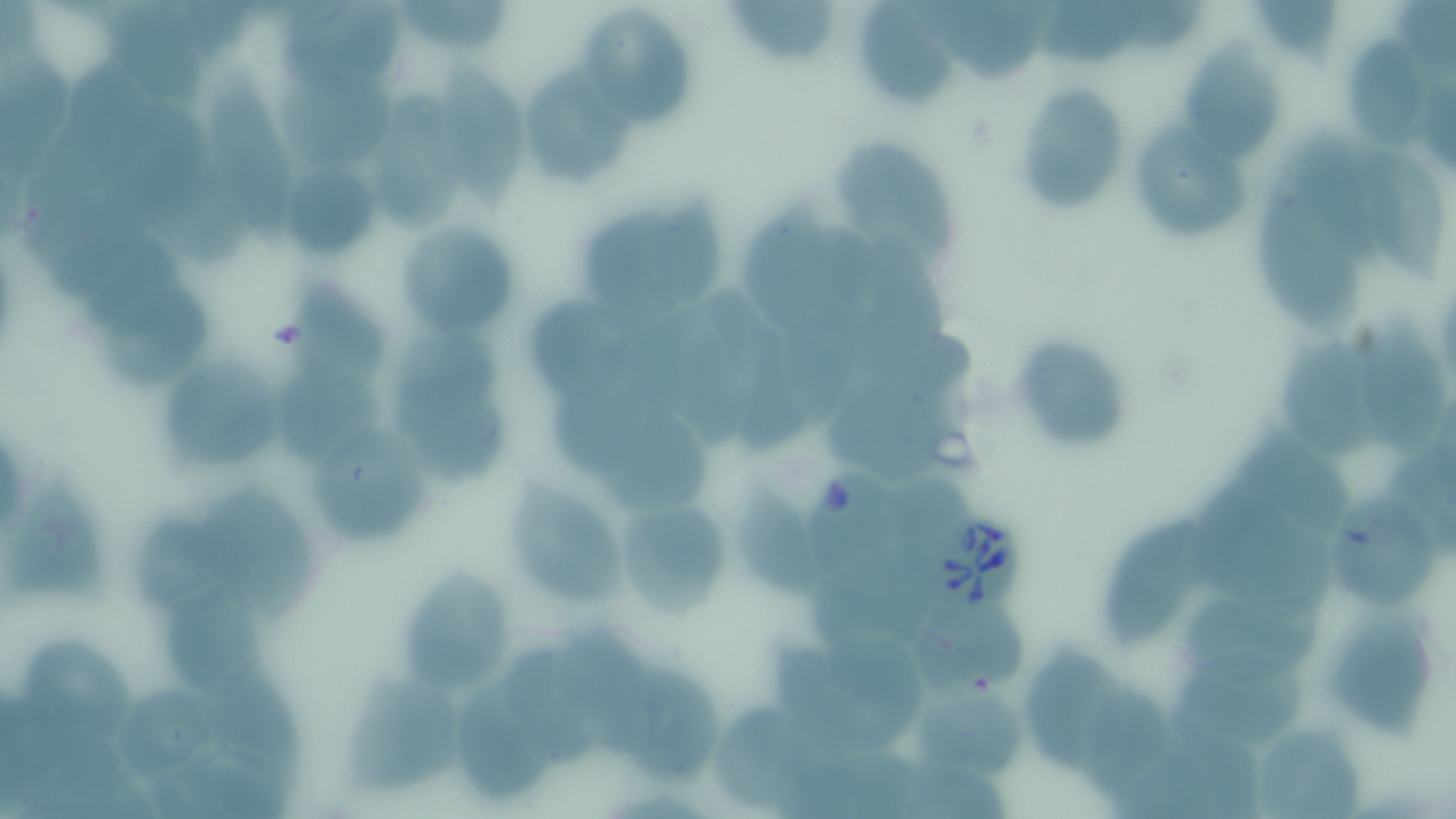 Approximate bounding boxes as [x1, y1, x2, y2] in pixels. Uninfected red blood cell locations: [105, 0, 204, 105], [723, 0, 844, 64], [931, 0, 1043, 84], [1037, 0, 1149, 69], [1258, 0, 1345, 69], [853, 1, 966, 104], [280, 3, 403, 87], [401, 3, 515, 53], [1114, 3, 1207, 51], [582, 6, 691, 126], [1346, 33, 1434, 149], [1173, 38, 1290, 161], [67, 54, 166, 173], [439, 58, 523, 214], [276, 61, 392, 168], [526, 64, 637, 183], [210, 67, 297, 259], [1010, 77, 1124, 212], [373, 93, 471, 229], [109, 98, 207, 219], [1135, 123, 1248, 240], [1294, 135, 1385, 273], [829, 138, 959, 262], [1342, 140, 1447, 283], [1255, 182, 1365, 331], [747, 195, 836, 333], [580, 197, 720, 305], [392, 218, 510, 334], [85, 226, 183, 327], [865, 237, 956, 379], [282, 279, 397, 388], [101, 280, 213, 387], [535, 293, 647, 400], [783, 298, 864, 424], [1364, 315, 1443, 460], [741, 325, 810, 455], [1284, 330, 1388, 465], [1012, 335, 1128, 450], [156, 351, 285, 472], [272, 365, 381, 464], [393, 371, 512, 484], [545, 379, 657, 476], [824, 393, 964, 482], [617, 398, 709, 522], [1235, 421, 1356, 538], [312, 423, 431, 546], [1192, 473, 1315, 587], [893, 475, 970, 567], [4, 479, 111, 604], [504, 480, 628, 607], [731, 481, 823, 602], [202, 486, 322, 625], [1321, 490, 1437, 607], [620, 502, 726, 625], [125, 510, 238, 620], [1101, 510, 1216, 649], [399, 565, 511, 692], [155, 593, 275, 698], [910, 593, 1035, 697], [1183, 593, 1323, 677], [1330, 606, 1435, 740], [816, 622, 927, 750], [558, 629, 643, 756], [1181, 637, 1310, 747], [19, 638, 142, 750], [497, 638, 593, 769], [1022, 638, 1132, 776], [771, 642, 872, 756], [605, 656, 719, 785], [197, 661, 315, 790], [338, 675, 467, 794], [117, 681, 210, 782], [457, 682, 551, 805], [1076, 682, 1174, 795], [917, 686, 1024, 781], [712, 703, 817, 809], [1248, 719, 1367, 817], [1138, 729, 1265, 817], [151, 749, 293, 819], [903, 765, 1011, 819]. Babesia divergens-infected red blood cell locations: [808, 470, 907, 585], [927, 511, 1025, 611]. Slide-level diagnosis: Babesia divergens. Image is 1456×819 pixels. May-Grünwald-Giemsa-stained preparation. Thin blood film. One field of a larger specimen. Light microscopy. Captured at 1000x magnification.